Describe the morphology of the erythrocytes.
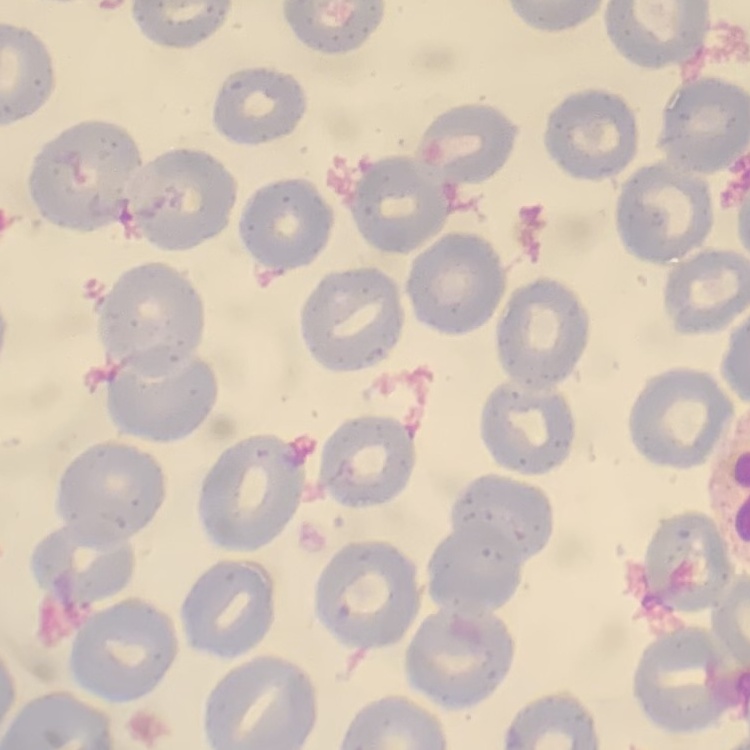

No rouleaux formation.

Summary:
  - Stain: Field's or Giemsa
  - Image type: square crop of a larger photomicrograph
  - Preparation: thin blood smear